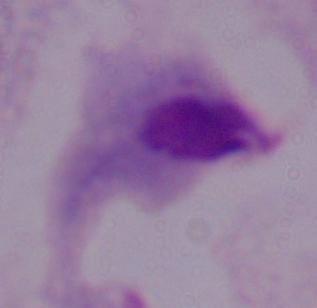

Summary:
  - Identification: trichomonad
  - Magnification: 1000x
  - Modality: micrograph